Report the malaria status of this cell.
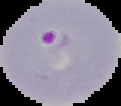
It is parasitized.

From a thin blood smear. Segmented cell region on a black background. Image is 121×106 pixels.